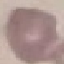
result: no malaria parasites detected
stain: Giemsa
preparation: thin smear
image_type: automatically extracted cell patch, resized to 64 × 64 pixels
capture: smartphone camera at the microscope eyepiece